Classify this cell by malaria status.
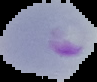

Parasitized.

Cell region segmented out of the field of view; the surrounding area is masked to black. Image is 97×82 pixels. From a thin blood smear.